Outline each blood parasite and name the species.
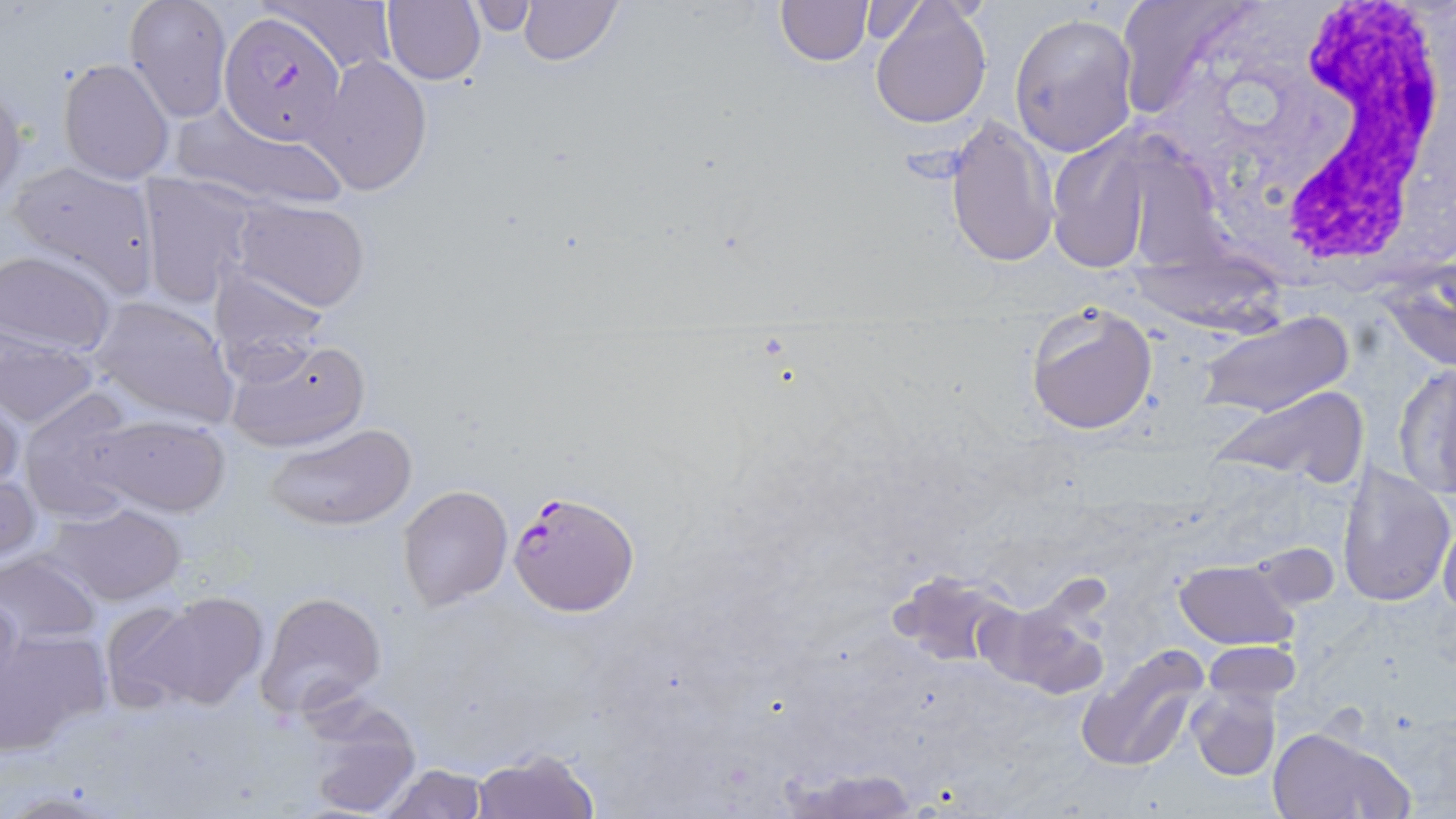
Approximate bounding boxes as (x1, y1, x2, y2) in pixels.
Plasmodium falciparum-infected red blood cells: (219, 10, 348, 147), (507, 490, 640, 616).
No Plasmodium ovale, Plasmodium malariae, Plasmodium vivax, Babesia divergens, or Trypanosoma brucei observed.

Summary:
  - Uninfected red blood cell locations: (124, 0, 233, 122), (267, 0, 398, 75), (381, 0, 485, 86), (517, 0, 622, 67), (774, 0, 872, 66), (1113, 0, 1259, 115), (465, 1, 540, 37), (869, 2, 992, 128), (1010, 12, 1139, 157), (309, 55, 432, 196), (57, 57, 175, 185), (0, 79, 25, 201), (172, 102, 350, 213), (945, 115, 1058, 268), (1042, 132, 1164, 274), (4, 159, 159, 299), (137, 175, 261, 306), (231, 199, 370, 313), (1, 251, 118, 357), (211, 269, 330, 380), (91, 297, 240, 430), (1024, 302, 1159, 435), (1194, 310, 1354, 420), (0, 332, 101, 430), (221, 334, 371, 454), (1393, 363, 1456, 498), (1210, 386, 1370, 484), (17, 388, 142, 525), (1, 391, 25, 497), (95, 415, 231, 517), (265, 423, 417, 530), (1336, 460, 1454, 608), (0, 471, 41, 565), (397, 484, 512, 612), (52, 502, 187, 605), (1439, 517, 1456, 618), (0, 552, 103, 647), (1175, 559, 1299, 649), (886, 570, 1022, 669), (253, 590, 388, 721), (129, 591, 270, 713), (0, 592, 23, 707), (975, 592, 1112, 700), (99, 598, 211, 711), (0, 628, 109, 752), (1201, 640, 1302, 703), (1077, 641, 1210, 772), (1186, 685, 1279, 780), (288, 691, 424, 818), (1267, 727, 1412, 819), (472, 748, 599, 819), (378, 764, 489, 818), (785, 766, 919, 819)
  - White blood cell locations: (1170, 9, 1453, 276)
  - Slide-level diagnosis: Plasmodium falciparum
  - Magnification: 1000x
  - Field of view: single
  - Image size: 1456×819 pixels
  - Stain: May-Grünwald-Giemsa
  - Preparation: thin blood smear
  - Modality: light microscopy